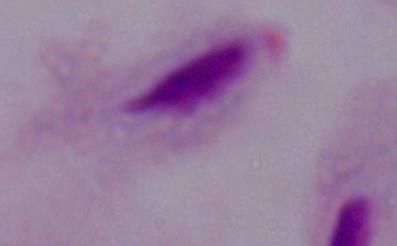

{
  "identification": "trichomonad",
  "modality": "micrograph",
  "magnification": "1000x"
}